Identify the cell.
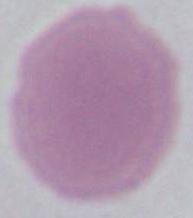
This is an erythrocyte.

Captured at 1000x magnification. Photomicrograph.